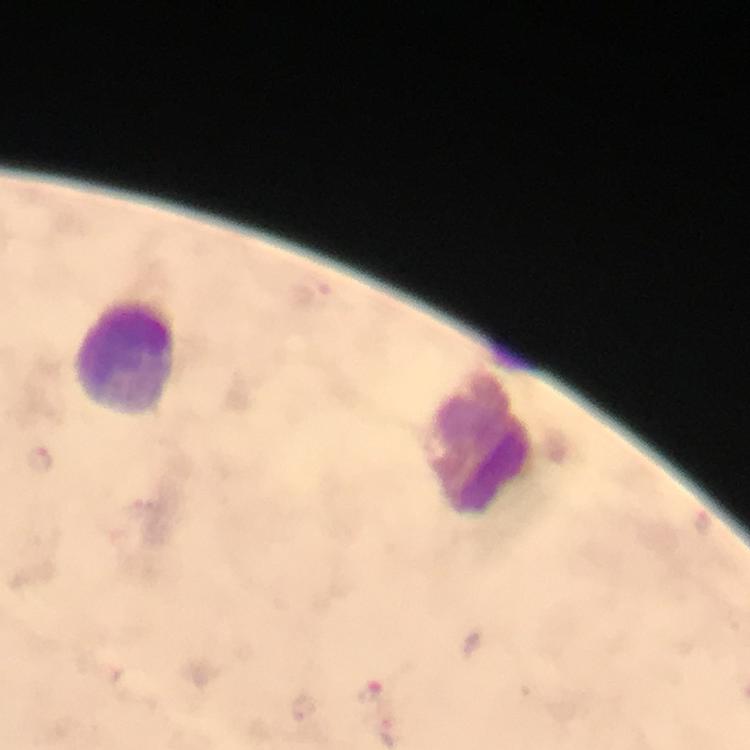

context: from a malaria diagnostic workup
image_size: 750×750 pixels
magnification: 100x
capture: smartphone photograph through a microscope
cropped_from: one field of view
plasmodium_parasite_locations: 'approximate centers as (x, y) in pixels: (40, 461), (371, 693)'
leukocyte_locations: 'approximate centers as (x, y) in pixels: (123, 360), (483, 445)'
immersion_oil: applied
stain: Giemsa
preparation: thick blood film